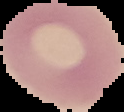
{
  "image_size": "124×112 pixels",
  "preparation": "thin blood film",
  "image_type": "segmented cell region with the area outside set to black",
  "result": "no malaria parasites seen"
}